Give the position of every malaria parasite.
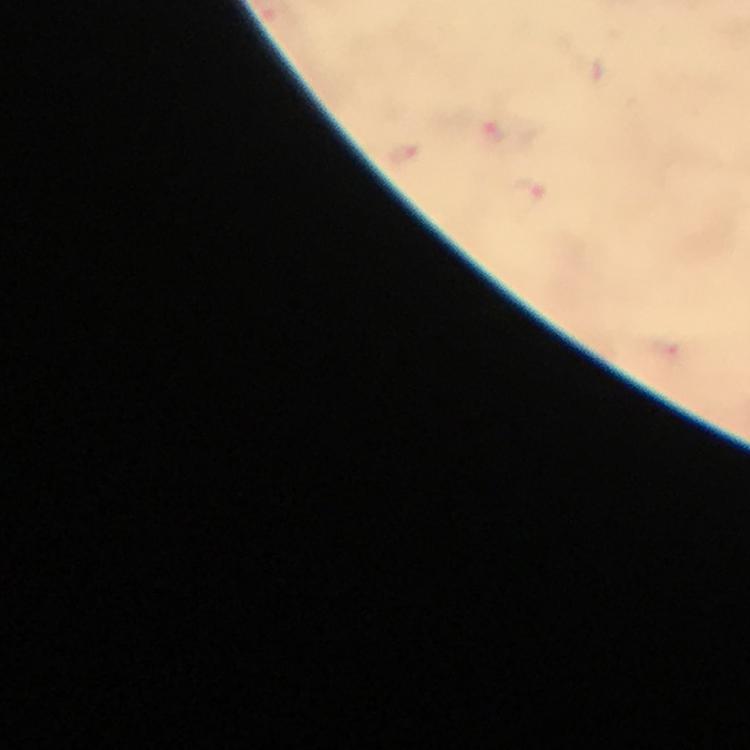

Approximate object centers, in pixels from the top-left corner.
Malaria parasites: (x=492, y=134), (x=403, y=151), (x=528, y=192).

Summary:
  - Cropped from: a single field of view
  - Immersion oil: used
  - Context: from a malaria diagnostic workup
  - Preparation: thick blood smear
  - Magnification: 100x
  - Capture: smartphone mounted on the microscope
  - Image size: 750×750 pixels
  - Stain: Giemsa